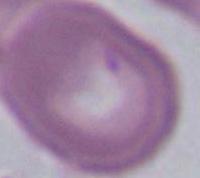

1000x magnification. An erythrocyte is seen. Micrograph.